Evaluate for malaria.
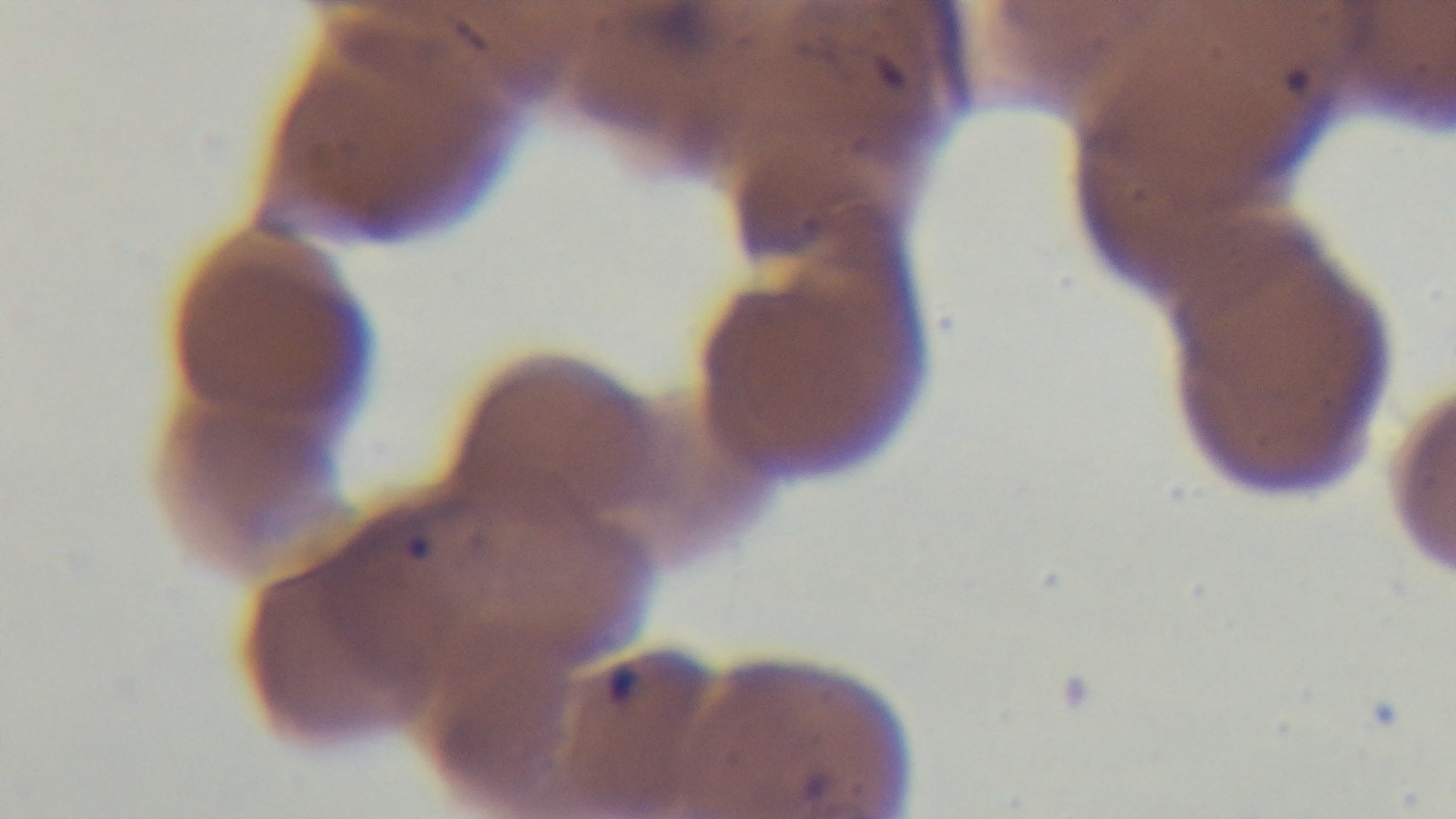
Positive.

Summary:
  - Preparation: thin
  - Stain: Giemsa
  - Field of view: one from the slide
  - Capture: mounted 4K digital camera
  - Objective: 100x oil immersion
  - Modality: light microscopy